Locate and identify every blood parasite.
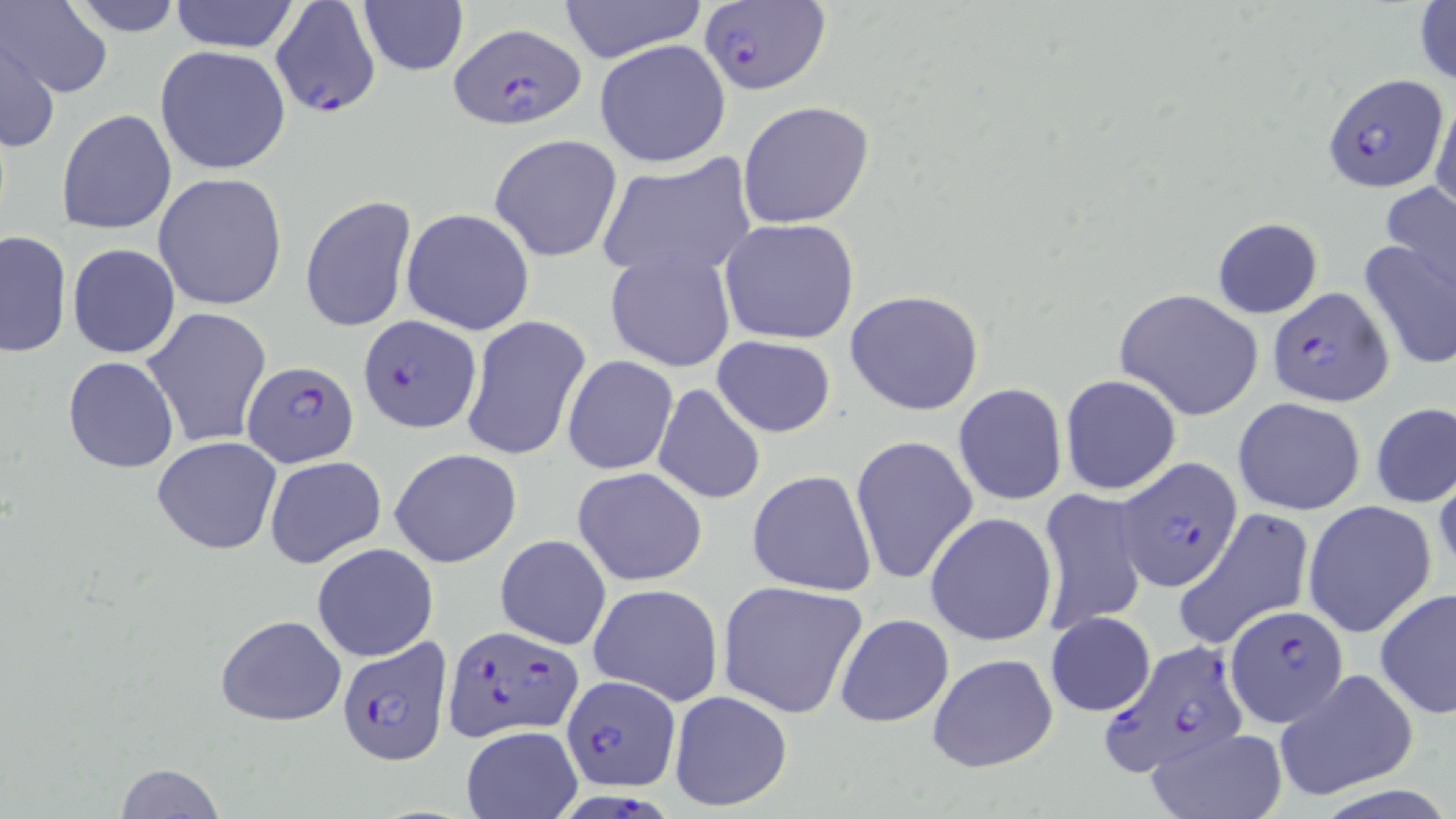

Approximate bounding boxes as named x1/y1/x2/y2 corners in pixels.
Plasmodium falciparum-infected red blood cells: (x1=269, y1=0, x2=380, y2=121), (x1=699, y1=1, x2=829, y2=94), (x1=448, y1=22, x2=586, y2=131), (x1=1322, y1=72, x2=1449, y2=192), (x1=1266, y1=286, x2=1393, y2=408), (x1=357, y1=314, x2=482, y2=434), (x1=242, y1=359, x2=359, y2=470), (x1=1115, y1=457, x2=1242, y2=591), (x1=1228, y1=604, x2=1348, y2=725), (x1=443, y1=624, x2=586, y2=743), (x1=336, y1=637, x2=451, y2=766), (x1=1099, y1=638, x2=1247, y2=777), (x1=560, y1=675, x2=680, y2=792), (x1=563, y1=790, x2=674, y2=819).
No Plasmodium ovale, Plasmodium malariae, Plasmodium vivax, Babesia divergens, or Trypanosoma brucei observed.

Uninfected red blood cell locations: (x1=3, y1=0, x2=112, y2=99), (x1=59, y1=0, x2=190, y2=35), (x1=167, y1=0, x2=302, y2=53), (x1=558, y1=0, x2=707, y2=62), (x1=357, y1=2, x2=469, y2=77), (x1=1414, y1=2, x2=1456, y2=89), (x1=2, y1=33, x2=60, y2=156), (x1=594, y1=39, x2=732, y2=169), (x1=153, y1=44, x2=293, y2=176), (x1=1431, y1=93, x2=1456, y2=216), (x1=737, y1=100, x2=876, y2=230), (x1=57, y1=108, x2=177, y2=236), (x1=488, y1=133, x2=624, y2=263), (x1=594, y1=156, x2=757, y2=282), (x1=153, y1=173, x2=288, y2=310), (x1=1379, y1=181, x2=1456, y2=297), (x1=300, y1=193, x2=417, y2=335), (x1=402, y1=207, x2=535, y2=335), (x1=1211, y1=216, x2=1324, y2=320), (x1=718, y1=218, x2=860, y2=345), (x1=0, y1=230, x2=71, y2=357), (x1=1358, y1=233, x2=1455, y2=373), (x1=67, y1=242, x2=180, y2=358), (x1=606, y1=247, x2=737, y2=372), (x1=844, y1=289, x2=986, y2=415), (x1=1115, y1=289, x2=1263, y2=420), (x1=141, y1=307, x2=273, y2=449), (x1=460, y1=316, x2=591, y2=463), (x1=711, y1=336, x2=837, y2=436), (x1=562, y1=355, x2=678, y2=476), (x1=63, y1=356, x2=179, y2=474), (x1=1060, y1=373, x2=1182, y2=495), (x1=651, y1=383, x2=766, y2=505), (x1=953, y1=383, x2=1067, y2=505), (x1=1234, y1=397, x2=1367, y2=515), (x1=1371, y1=402, x2=1456, y2=508), (x1=851, y1=436, x2=978, y2=587), (x1=152, y1=437, x2=282, y2=556), (x1=389, y1=448, x2=521, y2=567), (x1=263, y1=456, x2=387, y2=571), (x1=574, y1=466, x2=708, y2=585), (x1=746, y1=470, x2=877, y2=595), (x1=1035, y1=489, x2=1148, y2=634), (x1=1304, y1=501, x2=1437, y2=638), (x1=1176, y1=508, x2=1314, y2=650), (x1=924, y1=512, x2=1057, y2=645), (x1=495, y1=534, x2=611, y2=650), (x1=311, y1=542, x2=437, y2=662), (x1=717, y1=581, x2=867, y2=718), (x1=588, y1=583, x2=724, y2=707), (x1=1375, y1=588, x2=1456, y2=719), (x1=215, y1=612, x2=347, y2=725), (x1=1047, y1=612, x2=1155, y2=716), (x1=833, y1=613, x2=955, y2=728), (x1=925, y1=651, x2=1059, y2=774), (x1=1274, y1=670, x2=1417, y2=801), (x1=667, y1=689, x2=795, y2=814), (x1=461, y1=727, x2=582, y2=819), (x1=1145, y1=728, x2=1287, y2=819), (x1=111, y1=762, x2=226, y2=818). Slide-level diagnosis: Plasmodium falciparum. Image is 1456×819 pixels. Optical microscopy. Single field of view. Thin blood smear. Captured at 1000x magnification. May-Grünwald-Giemsa stain.